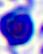

Summary:
  - Modality: photomicrograph
  - Magnification: 400x
  - Identification: white blood cell